Assess this cell for malaria.
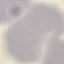

Uninfected.

Summary:
  - Image type: automatically extracted cell patch, resized to 64 × 64 pixels
  - Preparation: thin blood smear
  - Stain: Giemsa
  - Capture: smartphone through the microscope eyepiece